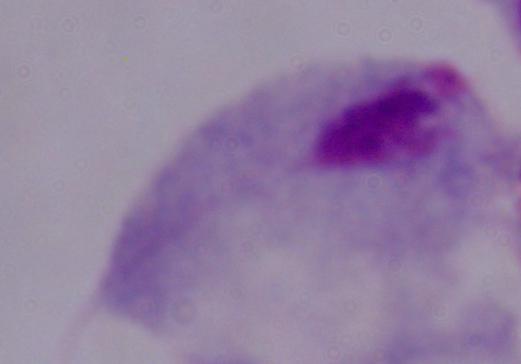

Summary:
  - Magnification: 1000x
  - Modality: photomicrograph
  - Identification: trichomonad